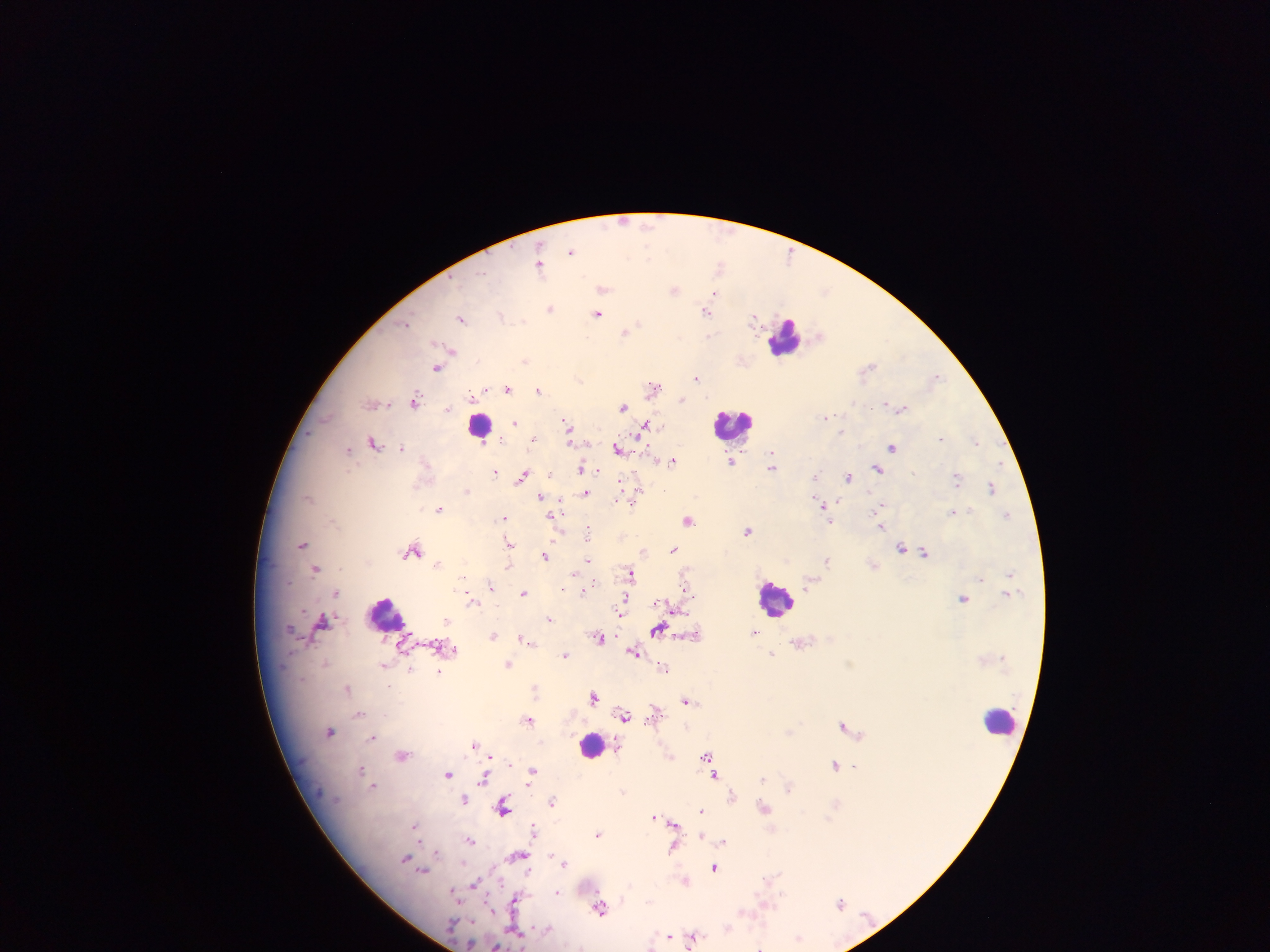

Approximate centers as [x, y] in pixels.
Summary:
  - Leukocyte locations: [785, 338], [733, 424], [481, 426], [776, 599], [386, 613], [1001, 719], [591, 746]
  - Plasmodium parasite locations: [571, 251], [791, 252], [540, 263], [720, 266], [602, 287], [675, 289], [717, 292], [551, 308], [707, 309], [599, 314], [502, 315], [754, 316], [462, 318], [406, 323], [627, 331], [451, 352], [527, 360], [741, 361], [438, 366], [868, 368], [697, 378], [936, 378], [654, 387], [509, 388], [539, 390], [414, 399], [473, 399], [682, 400], [374, 403], [624, 406], [900, 406], [825, 416], [514, 422], [567, 425], [646, 426], [842, 433], [503, 438], [533, 438], [942, 439], [374, 442], [976, 442], [892, 446], [402, 447], [619, 448], [349, 449], [772, 458], [673, 459], [732, 461], [772, 465], [582, 468], [878, 468], [496, 472], [524, 474], [550, 474], [816, 476], [849, 476], [958, 477], [621, 482], [992, 488], [467, 490], [639, 490], [586, 492], [542, 496], [619, 500], [630, 502], [824, 505], [883, 505], [441, 509], [954, 512], [1008, 514], [553, 516], [505, 518], [688, 519], [830, 519], [883, 525], [588, 530], [748, 530], [509, 541], [303, 543], [903, 548], [414, 549], [673, 549], [644, 551], [924, 552], [546, 556], [828, 559], [589, 560], [439, 563], [873, 565], [509, 566], [317, 568], [631, 573], [1009, 573], [981, 578], [490, 585], [584, 589], [562, 590], [338, 591], [524, 592], [1007, 593], [964, 598], [472, 599], [626, 602], [675, 607], [621, 612], [549, 618], [447, 619], [322, 620], [658, 629], [755, 632], [695, 634], [494, 635], [600, 637], [525, 639], [800, 642], [455, 648], [635, 650], [773, 654], [565, 655], [509, 662], [385, 664], [665, 668], [410, 669], [439, 670], [348, 688], [535, 688], [593, 696], [687, 700], [654, 713], [359, 714], [625, 715], [529, 719], [844, 725], [330, 731], [790, 732], [373, 737], [474, 744], [402, 754], [669, 756], [706, 756], [489, 757], [711, 762], [836, 765], [854, 765], [362, 769], [532, 772], [449, 773], [716, 774], [485, 778], [764, 778], [374, 785], [790, 786], [732, 795], [465, 797], [553, 801], [504, 807], [764, 807], [703, 811], [655, 815], [661, 817], [674, 823], [416, 826], [534, 830], [599, 834], [702, 836], [674, 838], [470, 840], [724, 841], [674, 845], [519, 854], [565, 862], [715, 867], [424, 869], [685, 880], [475, 883], [559, 892], [515, 898], [840, 903], [602, 907], [671, 936], [694, 936], [799, 938], [653, 945], [496, 946]
  - Capture: mobile-phone photograph through a microscope
  - Image size: 1270×952 pixels
  - Country: Ghana
  - Field of view: single
  - Preparation: thick blood smear